Name the blood parasite species.
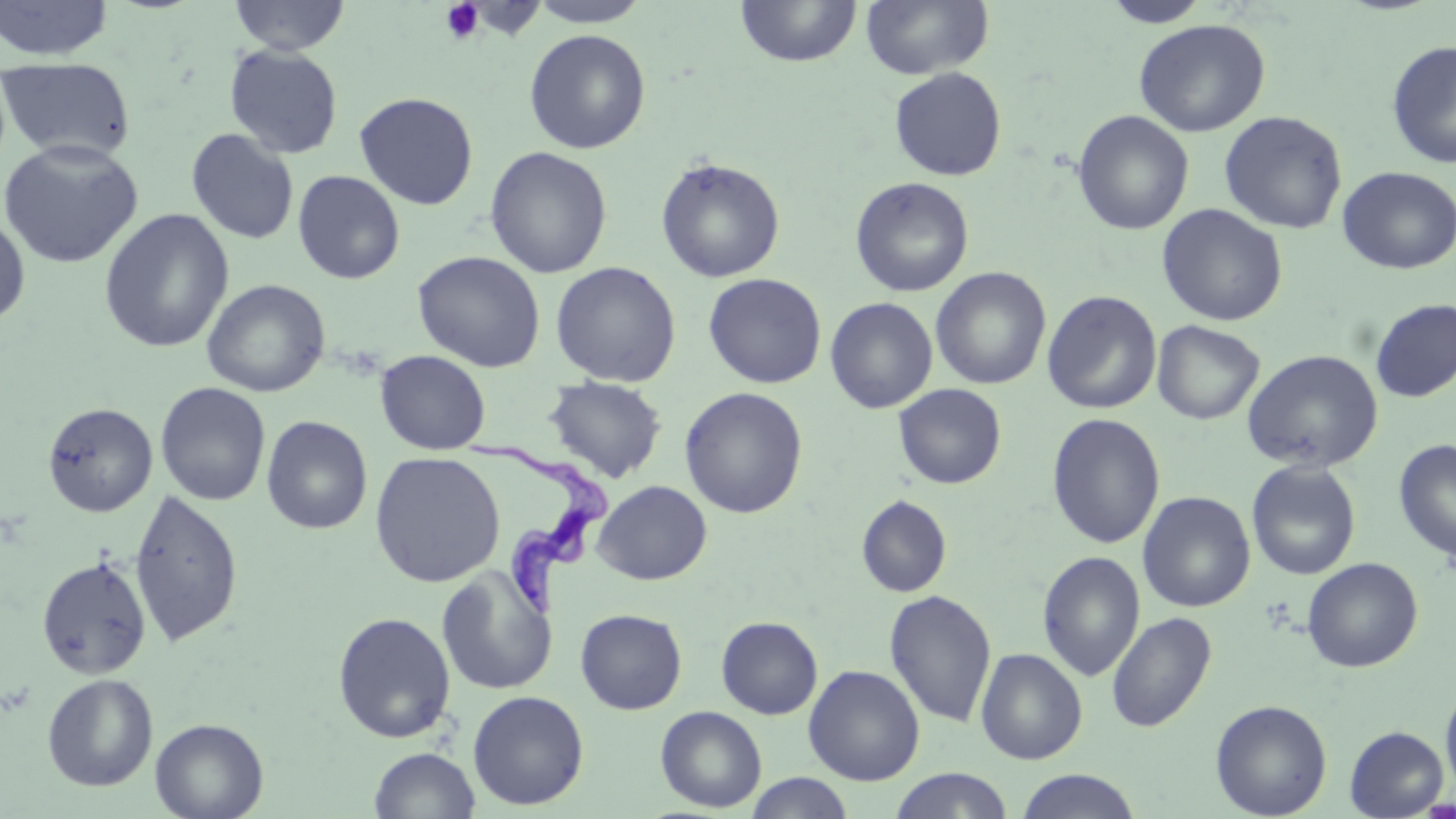
Trypanosoma brucei.

Summary:
  - Coordinate format: approximate bounding boxes as [x1, y1, x2, y2] in pixels
  - Uninfected red blood cell locations: [0, 0, 115, 61], [227, 0, 351, 55], [526, 0, 652, 28], [735, 0, 862, 67], [860, 0, 994, 80], [1101, 0, 1213, 28], [1133, 18, 1271, 137], [524, 29, 651, 154], [1385, 39, 1456, 169], [224, 45, 344, 159], [0, 57, 137, 163], [888, 66, 1007, 181], [354, 91, 479, 210], [1072, 110, 1193, 235], [1219, 111, 1347, 234], [185, 128, 299, 245], [0, 138, 144, 269], [485, 146, 612, 278], [655, 156, 785, 283], [1337, 166, 1456, 274], [293, 170, 405, 284], [850, 176, 974, 297], [1157, 204, 1287, 326], [98, 208, 234, 353], [0, 210, 31, 327], [412, 250, 546, 372], [550, 261, 681, 387], [930, 267, 1051, 390], [703, 272, 826, 389], [201, 279, 330, 397], [1043, 290, 1162, 414], [825, 297, 938, 414], [1370, 298, 1456, 403], [1152, 321, 1264, 424], [374, 350, 491, 455], [1242, 350, 1383, 472], [543, 376, 667, 483], [154, 382, 271, 506], [893, 383, 1007, 489], [679, 387, 808, 518], [42, 402, 157, 517], [1047, 413, 1165, 549], [261, 415, 373, 534], [1393, 438, 1456, 563], [369, 451, 505, 587], [1246, 460, 1362, 580], [592, 481, 712, 585], [129, 489, 243, 649], [1137, 492, 1255, 613], [857, 495, 952, 597], [1038, 551, 1145, 683], [35, 555, 152, 679], [1302, 557, 1422, 672], [436, 568, 557, 695], [884, 589, 997, 728], [575, 608, 687, 714], [332, 612, 456, 744], [1106, 612, 1216, 733], [716, 616, 823, 719], [975, 648, 1088, 764], [803, 664, 925, 785], [42, 673, 158, 791], [1441, 684, 1456, 796], [467, 690, 589, 810], [1210, 699, 1332, 818], [655, 706, 767, 812], [150, 717, 269, 819], [1344, 726, 1449, 817], [369, 747, 481, 819], [888, 769, 1015, 819], [1014, 769, 1142, 818], [744, 773, 855, 819]
  - Trypanosoma brucei locations: [466, 433, 615, 626]
  - Platelet locations: [440, 0, 486, 44]
  - Preparation: thin blood film
  - Image size: 1456×819 pixels
  - Stain: May-Grünwald-Giemsa
  - Modality: optical microscopy
  - Magnification: 1000x
  - Field of view: single